Report the malaria status of this cell.
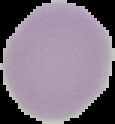

It is uninfected.

{
  "preparation": "thin blood smear",
  "image_size": "115×124 pixels",
  "image_type": "cell region segmented out of the field of view; surrounding area masked to black"
}